Describe the morphology of the erythrocytes.
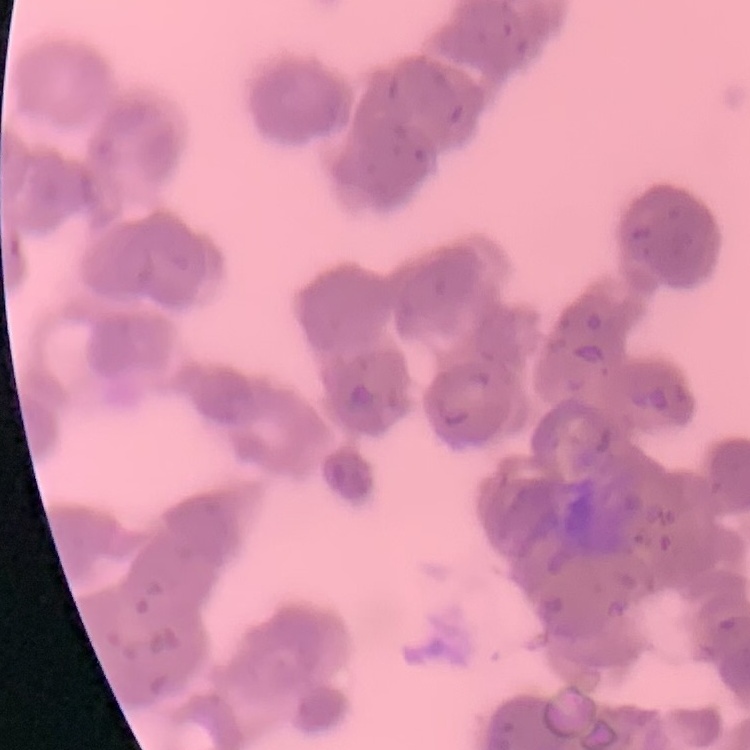
They show rouleaux formation.

image type = square crop of a larger photomicrograph
preparation = thin peripheral smear
stain = Field's or Giemsa